Identify the parasite.
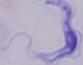
This is a trypanosome.

modality = photomicrograph
magnification = 1000x